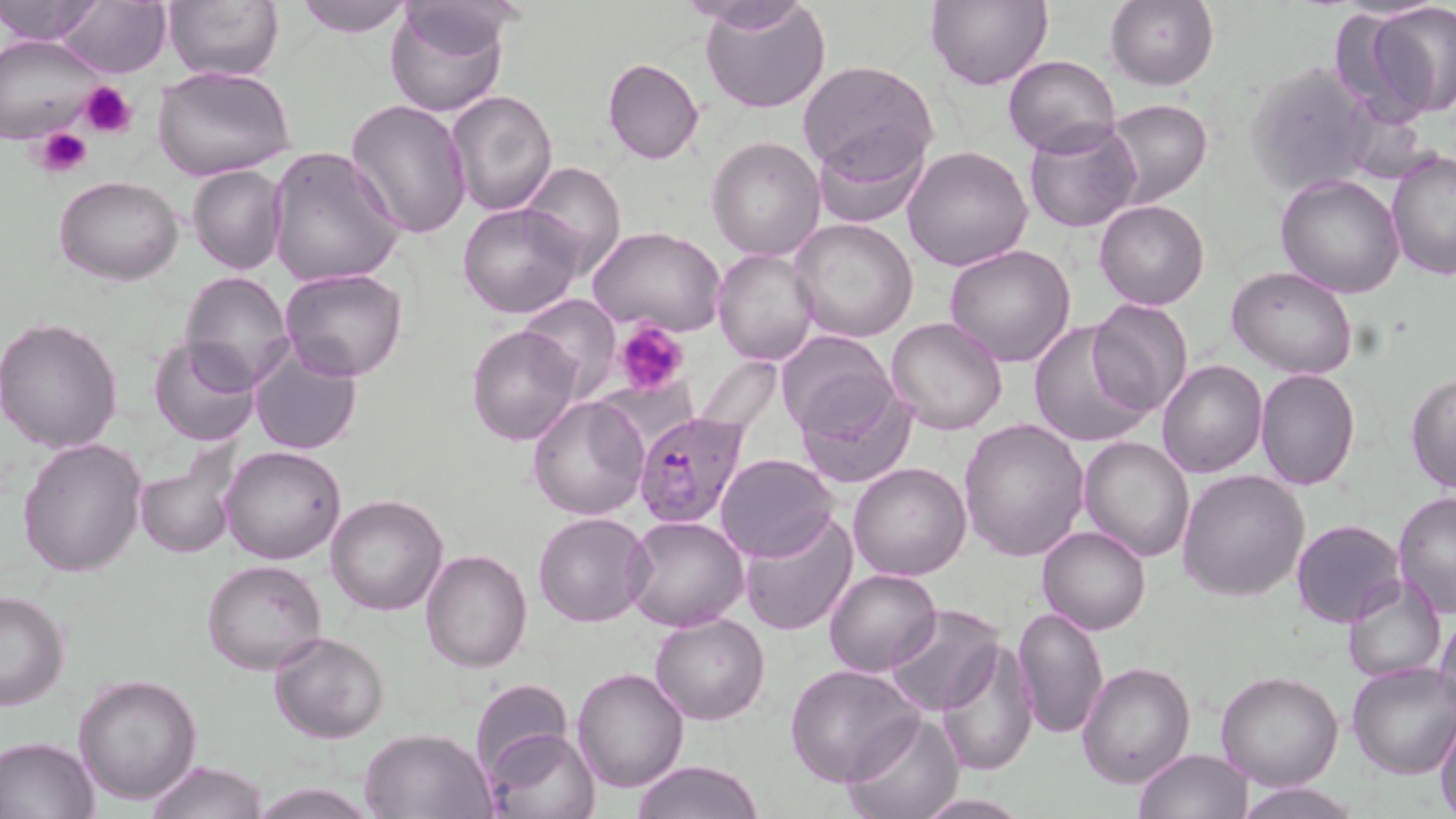
Summary:
  - Coordinate format: approximate bounding boxes as (x1,y1)-(x2,y2) corner pairs in pixels
  - Uninfected red blood cell locations: (0,0)-(103,45), (55,0)-(171,78), (162,0)-(286,81), (294,0)-(415,35), (683,0)-(811,33), (700,0)-(831,115), (928,0)-(1053,91), (1104,0)-(1219,89), (384,3)-(510,117), (1361,5)-(1455,124), (0,36)-(104,144), (1004,55)-(1120,157), (602,58)-(704,165), (1244,60)-(1378,198), (796,61)-(938,180), (153,64)-(298,182), (445,88)-(559,215), (345,97)-(473,240), (1101,97)-(1213,208), (1025,120)-(1143,233), (811,127)-(929,228), (707,135)-(825,259), (902,144)-(1033,273), (266,145)-(406,290), (1386,149)-(1456,279), (520,161)-(626,278), (187,165)-(289,276), (1275,174)-(1406,299), (56,176)-(184,286), (457,200)-(585,318), (1094,200)-(1210,311), (791,217)-(919,342), (587,225)-(727,336), (944,245)-(1076,367), (713,247)-(820,365), (1227,266)-(1358,380), (280,268)-(407,381), (178,271)-(296,392), (518,293)-(618,401), (1087,298)-(1195,419), (0,315)-(124,453), (884,317)-(1009,436), (1027,320)-(1153,451), (467,323)-(583,446), (776,330)-(896,443), (148,338)-(260,447), (248,341)-(362,456), (1156,360)-(1266,478), (1256,369)-(1360,490), (1405,373)-(1456,494), (794,376)-(917,490), (528,395)-(650,521), (959,418)-(1090,560), (1079,434)-(1195,560), (17,436)-(149,579), (133,445)-(243,559), (221,446)-(348,564), (715,453)-(837,561), (848,461)-(972,582), (1178,470)-(1309,601), (1392,490)-(1456,621), (325,494)-(449,616), (533,511)-(653,627), (739,513)-(858,636), (621,515)-(750,632), (1290,519)-(1406,627), (1038,525)-(1151,634), (421,548)-(532,673), (201,559)-(327,674), (824,568)-(941,674), (1341,576)-(1447,683), (0,590)-(70,710), (882,603)-(1003,717), (1013,605)-(1107,742), (1435,605)-(1456,722), (651,611)-(770,725), (271,631)-(389,743), (938,640)-(1038,775), (1078,662)-(1195,786), (1347,662)-(1456,778), (784,665)-(923,786), (573,667)-(689,792), (1215,672)-(1343,791), (73,674)-(202,805), (470,678)-(573,780), (840,711)-(963,818), (1434,718)-(1456,819), (482,726)-(598,819), (360,727)-(495,817), (0,735)-(101,818), (1133,748)-(1252,818), (633,759)-(765,818), (145,761)-(268,819), (248,782)-(379,818), (1234,783)-(1364,818), (912,796)-(1033,817)
  - Plasmodium falciparum-infected red blood cell locations: (632,411)-(750,531)
  - Platelet locations: (79,82)-(138,139), (36,127)-(92,179), (615,319)-(688,397)
  - Slide-level diagnosis: Plasmodium falciparum
  - Image size: 1456×819 pixels
  - Preparation: thin blood smear
  - Stain: May-Grünwald-Giemsa
  - Field of view: single
  - Modality: light microscopy
  - Magnification: 1000x